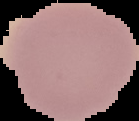 From a thin blood smear. Image is 139×121 pixels. Segmented cell region on a black background. Result: negative for malaria parasites.